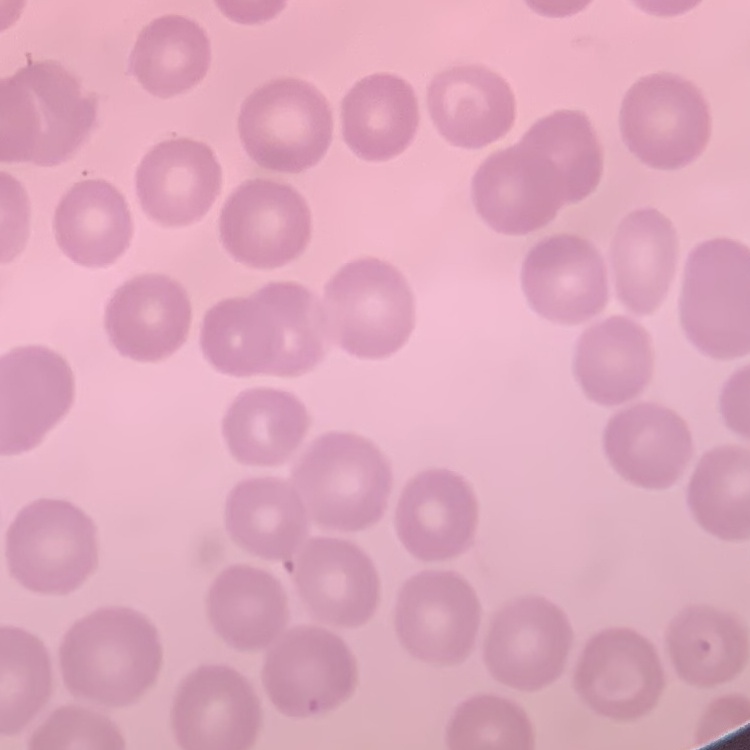
red blood cell morphology = no rouleaux formation
image type = one tile cut from a larger photomicrograph
preparation = thin peripheral smear
stain = Field's or Giemsa